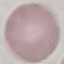 Malaria status: uninfected. Automatically extracted cell patch, resized to 64 × 64 pixels. Acquired by smartphone through the microscope eyepiece. Thin blood smear. Giemsa-stained preparation.